Comment on the morphology of the red blood cells.
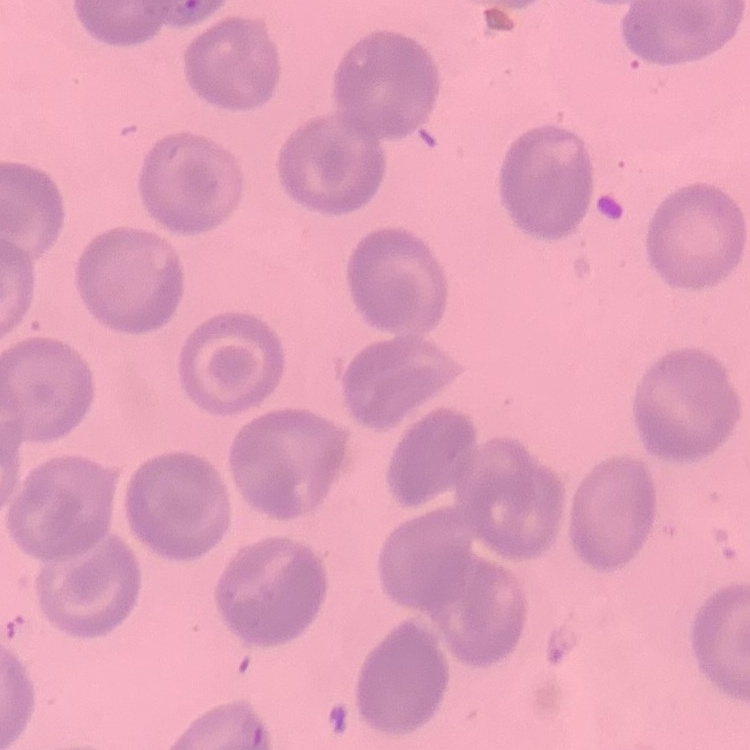
They show no rouleaux formation.

Field's or Giemsa stain. Thin blood film. Square crop of a larger photomicrograph.